State the preparation type.
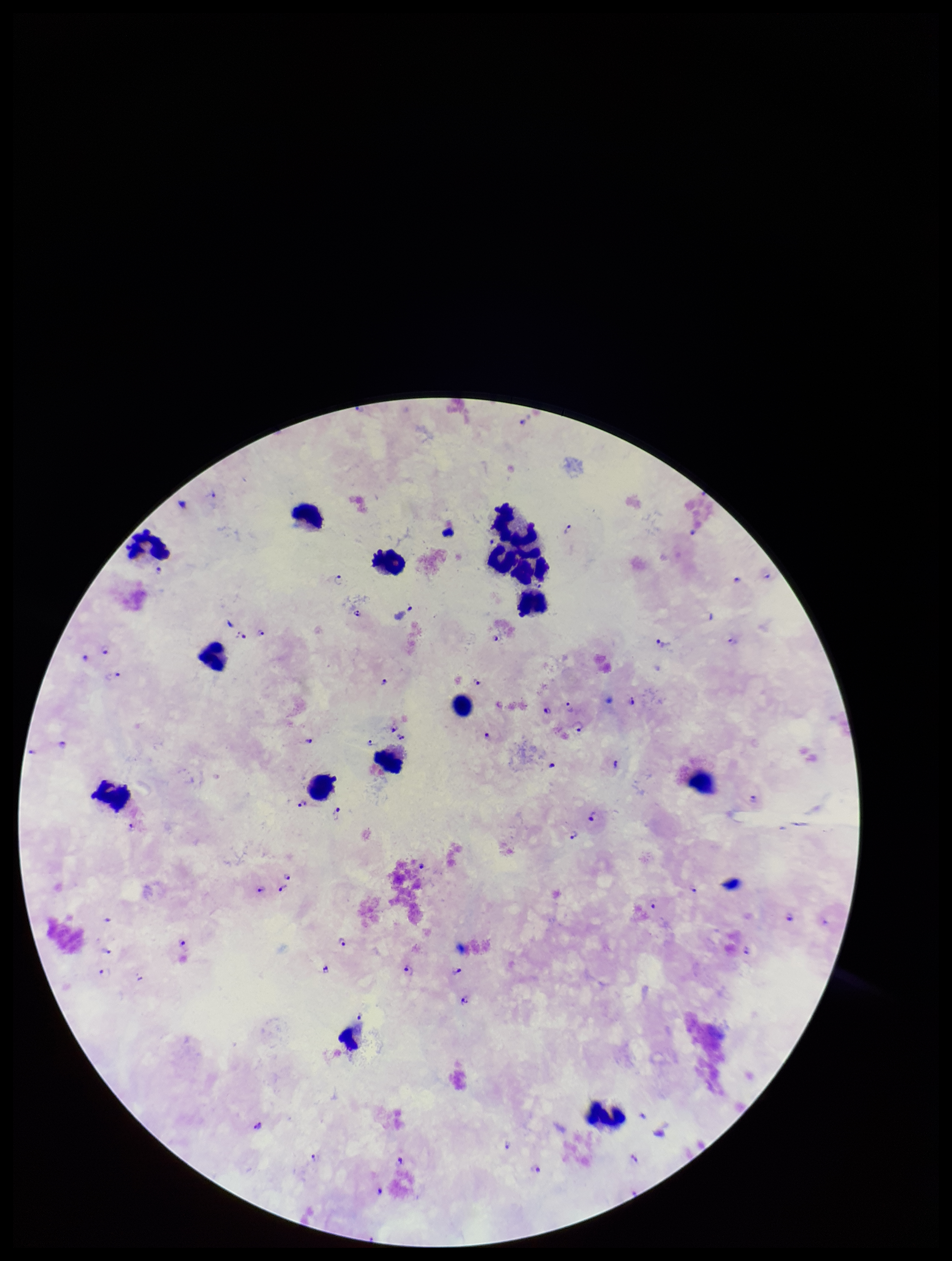

Thick.

Image is 952×1261 pixels. Parasite count: 51. Stained with Giemsa. One field from this slide. Leukocyte count: 15. Smartphone photograph taken through the eyepiece of a microscope. Patient malaria status: positive. Plasmodium parasites: seen. Species reported for this patient: Plasmodium falciparum.